State which cell type is depicted.
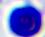

A leukocyte.

magnification = 400x
modality = micrograph